Report the malaria status of this cell.
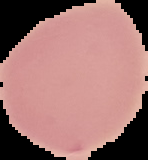
It is uninfected.

image size = 148×160 pixels
image type = cell region segmented out of the field of view; surrounding area masked to black
preparation = thin blood smear